Describe the morphology of the red blood cells.
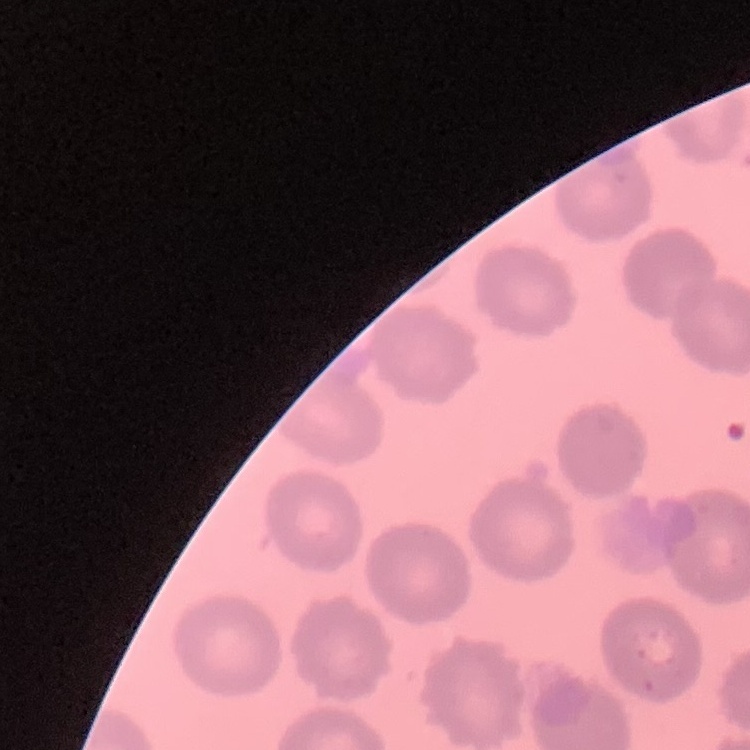

They show no rouleaux formation.

Summary:
  - Image type: square crop of a larger photomicrograph
  - Preparation: thin peripheral smear
  - Stain: Field's or Giemsa